Locate and identify every blood parasite.
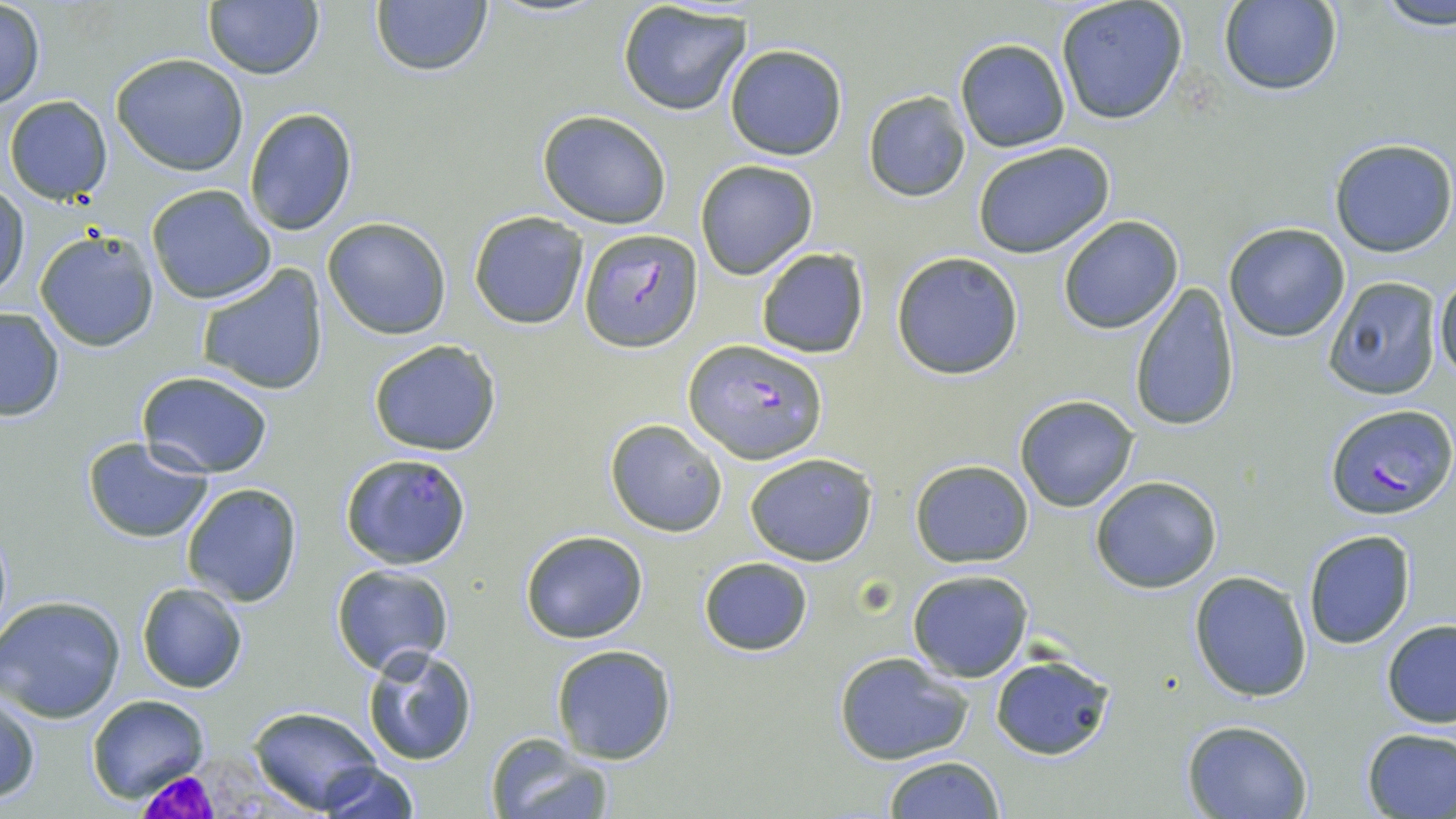
Approximate bounding boxes as (x1, y1, x2, y2) in pixels.
Plasmodium falciparum-infected red blood cells: (579, 226, 700, 351), (685, 339, 824, 462), (1324, 403, 1455, 519), (335, 453, 466, 568).
No Plasmodium ovale, Plasmodium malariae, Plasmodium vivax, Babesia divergens, or Trypanosoma brucei observed.

Uninfected red blood cell locations: (1376, 0, 1456, 32), (201, 1, 325, 81), (370, 1, 493, 79), (1054, 1, 1188, 126), (1217, 1, 1342, 96), (0, 2, 45, 107), (617, 2, 752, 116), (953, 37, 1071, 153), (724, 43, 848, 160), (110, 53, 249, 175), (863, 91, 970, 202), (4, 96, 112, 205), (242, 107, 359, 234), (537, 109, 672, 229), (1328, 137, 1455, 258), (971, 141, 1115, 258), (694, 159, 818, 279), (146, 184, 278, 303), (1, 185, 28, 301), (469, 210, 589, 329), (1057, 215, 1184, 334), (322, 216, 452, 340), (1223, 221, 1350, 343), (33, 229, 160, 353), (754, 246, 869, 359), (891, 252, 1023, 377), (196, 264, 328, 395), (1434, 269, 1456, 385), (1322, 276, 1442, 401), (1128, 282, 1241, 432), (0, 308, 65, 421), (368, 340, 502, 457), (137, 369, 273, 478), (1014, 395, 1139, 512), (604, 419, 727, 537), (81, 436, 214, 542), (745, 452, 878, 566), (909, 460, 1034, 569), (1090, 475, 1222, 592), (181, 483, 304, 608), (519, 530, 649, 644), (1302, 531, 1415, 648), (697, 556, 815, 656), (330, 563, 455, 676), (906, 569, 1032, 681), (1189, 570, 1313, 702), (137, 582, 249, 694), (0, 594, 128, 723), (1381, 619, 1456, 728), (550, 644, 678, 765), (360, 645, 479, 767), (833, 651, 977, 766), (989, 655, 1116, 761), (1, 692, 41, 805), (88, 694, 210, 804), (248, 707, 388, 814), (1181, 718, 1314, 818), (1360, 727, 1456, 818), (484, 735, 615, 819), (883, 755, 1005, 817), (317, 763, 417, 819). White blood cell locations: (125, 753, 324, 818). Slide-level diagnosis: Plasmodium falciparum. Captured at 1000x magnification. May-Grünwald-Giemsa-stained preparation. Single field of view. Thin blood film. Light microscopy. Image is 1456×819 pixels.